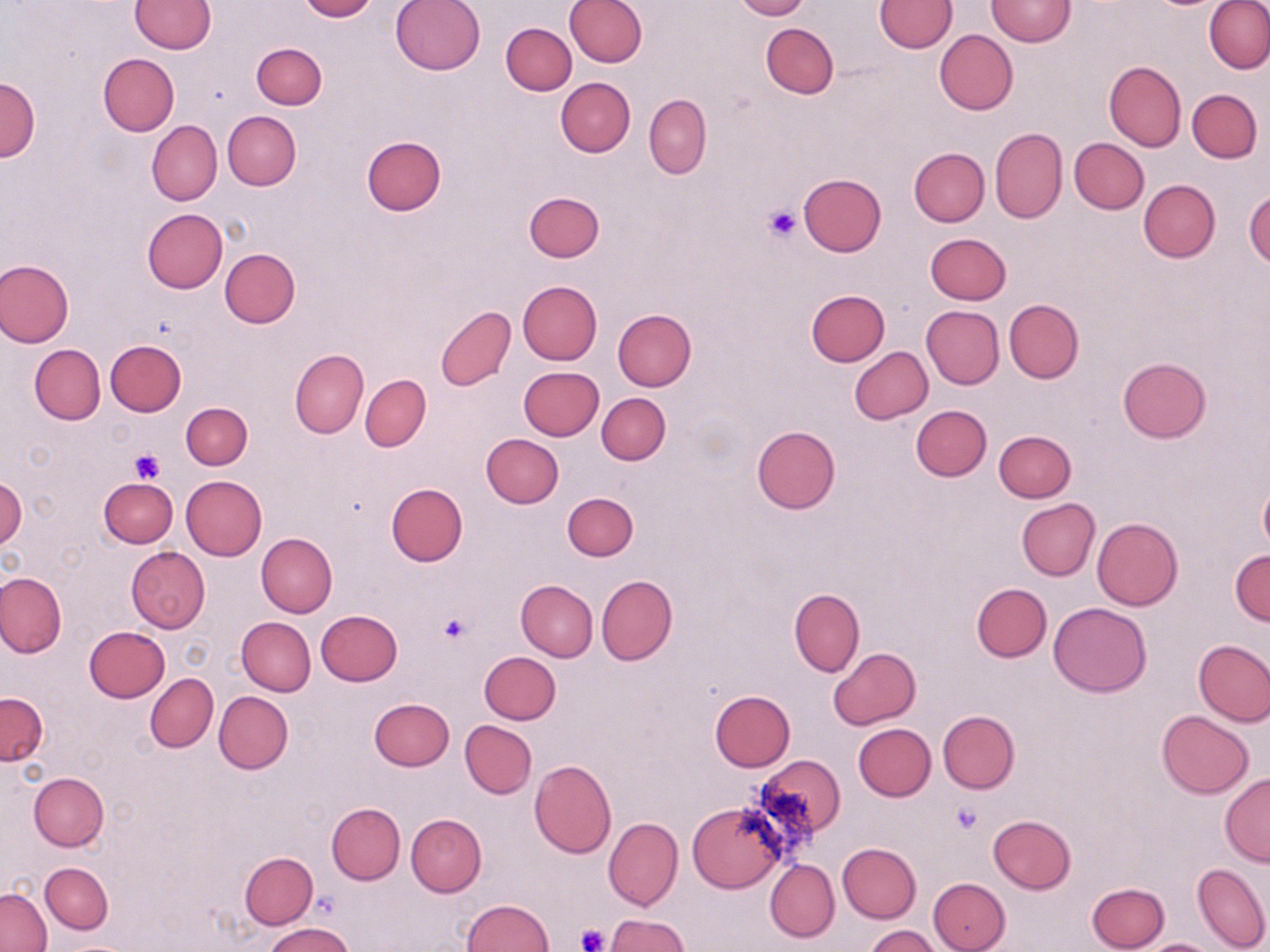
Approximate bounding boxes as (x1,y1)-(x2,y2) corner pairs in pixels. Uninfected red blood cell locations: (131,0)-(215,53), (299,0)-(377,21), (390,0)-(486,75), (563,0)-(647,66), (733,0)-(808,20), (875,0)-(955,52), (986,0)-(1074,47), (1204,0)-(1270,75), (500,23)-(576,95), (761,23)-(838,98), (933,29)-(1018,115), (252,42)-(326,109), (98,54)-(178,136), (1104,61)-(1186,152), (1,78)-(40,161), (556,78)-(636,157), (1188,88)-(1262,162), (644,94)-(711,178), (222,110)-(301,191), (147,121)-(222,205), (989,128)-(1067,223), (360,134)-(446,215), (1068,138)-(1148,215), (909,148)-(988,226), (797,174)-(887,256), (1138,179)-(1220,261), (1244,190)-(1270,268), (524,191)-(604,262), (143,208)-(227,293), (925,232)-(1011,305), (220,249)-(299,328), (0,258)-(74,349), (518,280)-(602,364), (804,289)-(889,367), (1004,300)-(1083,383), (921,305)-(1003,389), (435,307)-(516,390), (612,308)-(696,390), (105,339)-(186,415), (30,344)-(105,425), (849,347)-(933,424), (289,349)-(368,438), (1117,356)-(1209,442), (518,366)-(603,440), (361,375)-(431,450), (597,392)-(669,465), (180,402)-(253,470), (911,404)-(991,481), (752,426)-(840,513), (994,431)-(1076,502), (480,433)-(563,508), (181,475)-(267,560), (0,477)-(25,552), (98,478)-(178,548), (1258,481)-(1270,554), (385,482)-(468,566), (562,493)-(638,561), (1016,499)-(1099,580), (1091,518)-(1184,611), (257,533)-(337,617), (126,546)-(210,633), (1231,551)-(1270,626), (0,571)-(66,659), (596,575)-(677,665), (516,579)-(598,661), (971,583)-(1051,661), (789,588)-(865,676), (1048,602)-(1151,697), (316,610)-(403,685), (237,617)-(316,696), (84,626)-(170,702), (1193,639)-(1270,727), (828,647)-(922,730), (479,651)-(560,724), (145,673)-(218,752), (709,690)-(795,771), (213,691)-(292,774), (0,692)-(47,765), (369,698)-(454,771), (1156,710)-(1254,798), (938,711)-(1020,794), (460,720)-(537,797), (854,723)-(935,800), (755,755)-(845,842), (529,760)-(617,858), (29,772)-(108,851), (1220,774)-(1270,866), (327,803)-(405,884), (688,804)-(785,892), (406,813)-(486,896), (988,815)-(1077,893), (604,817)-(683,910), (836,842)-(921,923), (240,852)-(318,928), (765,859)-(840,942), (40,862)-(113,934), (1192,863)-(1269,952), (928,877)-(1010,952), (1087,881)-(1170,951), (0,888)-(51,952), (461,898)-(552,951), (603,913)-(689,952), (265,922)-(356,952), (864,925)-(941,952), (1136,938)-(1221,952). Platelet locations: (763,204)-(800,243), (129,447)-(165,484), (438,612)-(474,645), (950,802)-(984,835), (573,924)-(610,952). Slide-level diagnosis: negative for blood parasites. Single field of view. Image is 1270×952 pixels. Light microscopy. Thin blood smear. May-Grünwald-Giemsa-stained preparation. Captured at 1000x magnification.